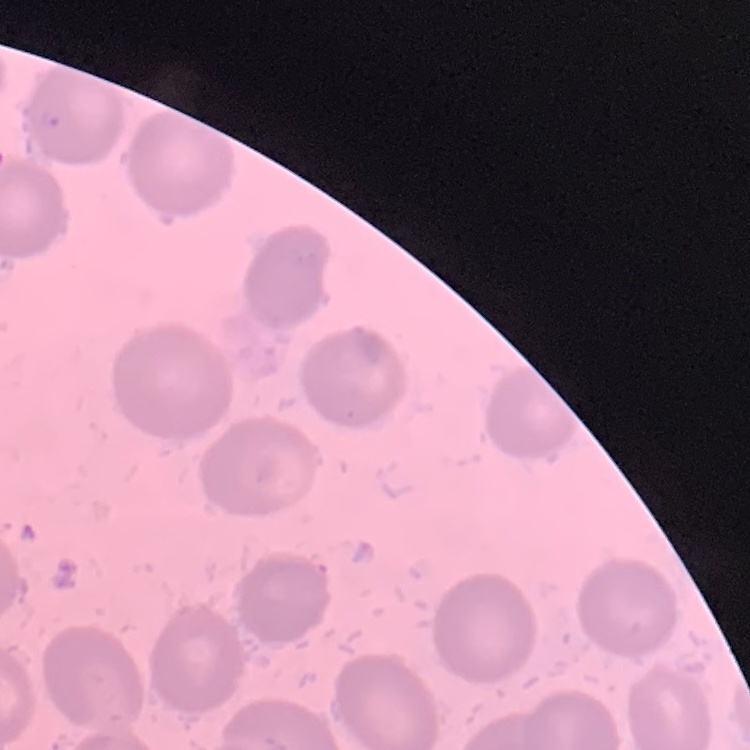

erythrocyte_morphology: no rouleaux formation
preparation: thin peripheral smear
image_type: square crop of a larger photomicrograph
stain: Field's or Giemsa